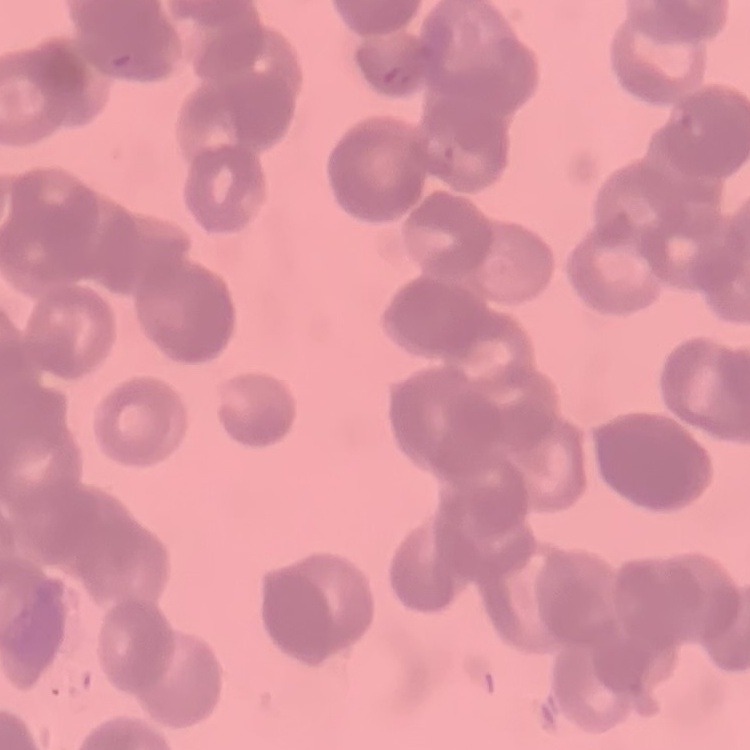
red_blood_cell_morphology: rouleaux formation
image_type: one tile cut from a larger photomicrograph
stain: Field's or Giemsa
preparation: thin blood smear